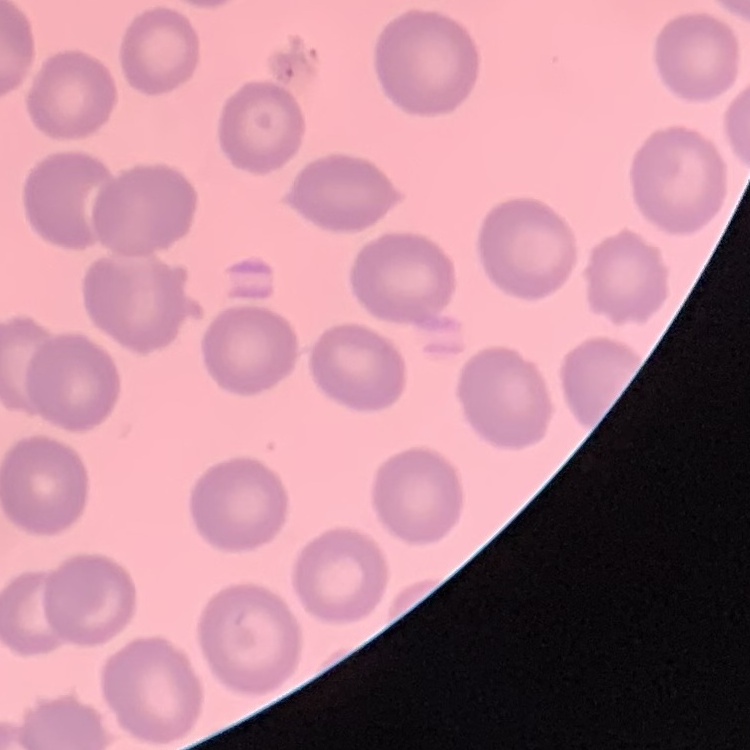 The red blood cells show no rouleaux formation. Thin blood smear. One tile cut from a larger photomicrograph. Field's or Giemsa stain.